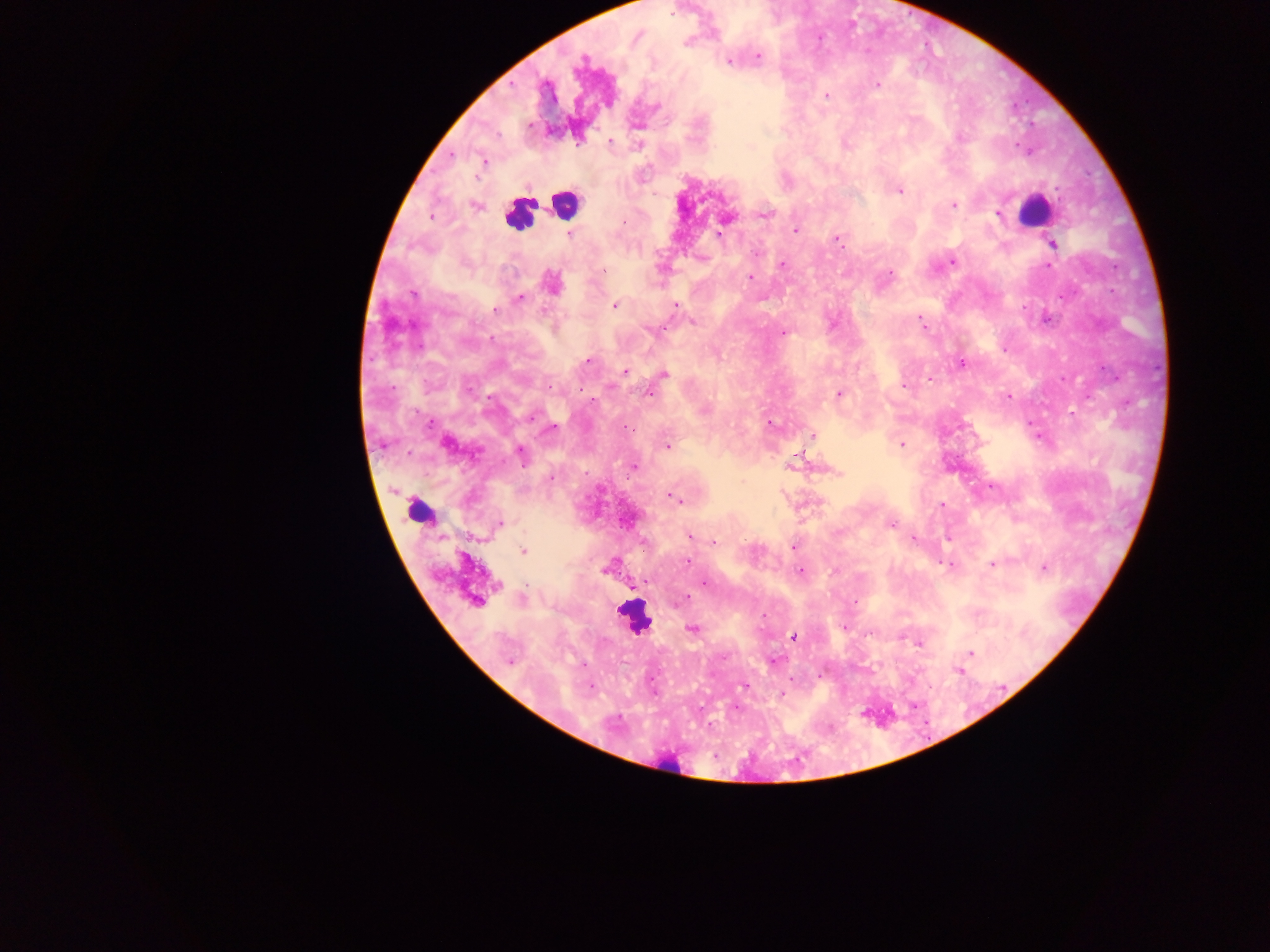
malaria_parasite_locations: 'approximate centers as (x, y) in pixels: (757, 56), (728, 61), (580, 62), (877, 85), (826, 96), (528, 126), (610, 142), (639, 145), (484, 161), (899, 191), (954, 205), (475, 206), (998, 213), (764, 215), (430, 216), (796, 231), (570, 233), (718, 236), (838, 240), (1053, 244), (756, 254), (953, 262), (783, 264), (603, 270), (890, 273), (749, 278), (552, 283), (412, 293), (519, 299), (615, 305), (675, 305), (495, 311), (693, 321), (922, 323), (783, 333), (586, 361), (962, 364), (624, 372), (663, 374), (930, 379), (904, 386), (649, 394), (839, 394), (1009, 396), (770, 424), (553, 428), (628, 428), (811, 435), (446, 444), (901, 445), (668, 446), (521, 454), (792, 466), (633, 467), (837, 473), (550, 477), (674, 497), (943, 505), (500, 524), (891, 524), (689, 537), (915, 540), (714, 542), (794, 547), (523, 552), (688, 563), (992, 564), (950, 565), (1044, 568), (606, 570), (800, 572), (704, 584), (498, 585), (685, 598), (523, 599), (476, 601), (692, 628), (793, 637), (918, 643), (971, 653), (510, 662), (958, 670), (744, 686)'
capture: mobile-phone photograph through a microscope
preparation: thick blood film
country: Ghana
image_size: 1270×952 pixels
leukocyte_locations: 'approximate centers as (x, y) in pixels: (564, 203), (1032, 205), (519, 215), (422, 512), (634, 618), (676, 762)'
field_of_view: single